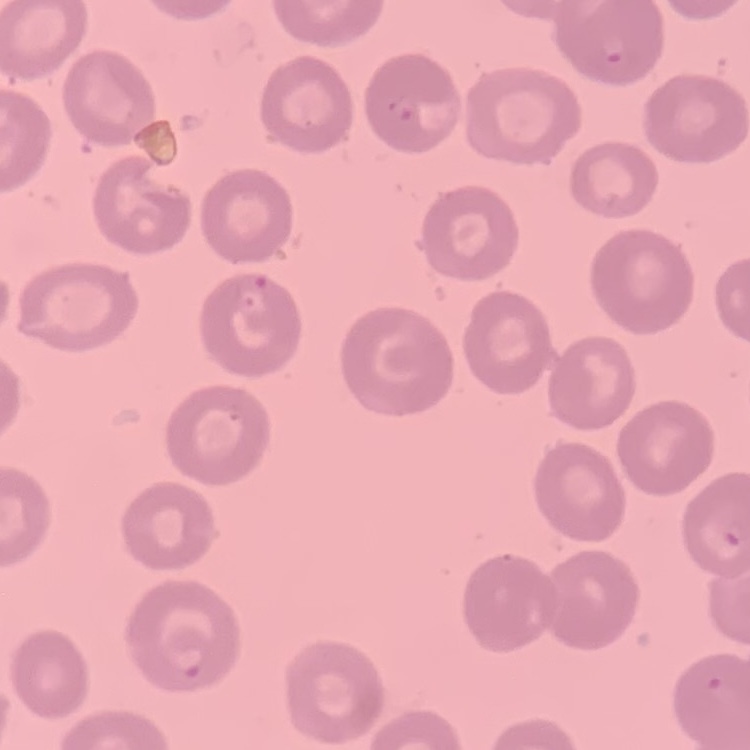

The red blood cells show no rouleaux formation. Stained with either Field's or Giemsa. Thin peripheral smear. Square crop of a larger photomicrograph.